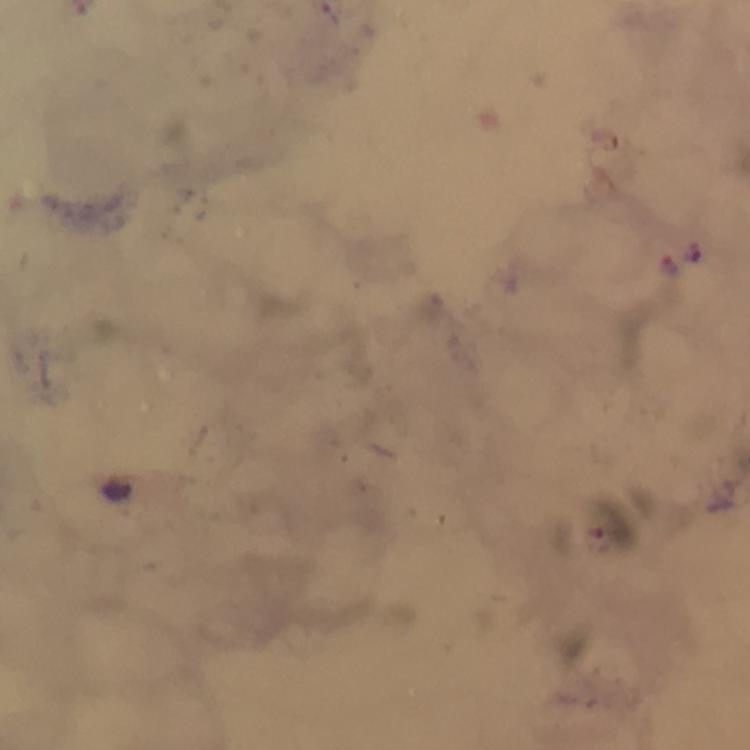
capture: smartphone camera through the microscope
immersion_oil: applied
plasmodium_parasite_locations: 'approximate centers as (x, y) in pixels: (667, 265)'
cropped_from: a single field of view
context: from a malaria diagnostic workup
preparation: thick blood smear
magnification: 100x
image_size: 750×750 pixels
stain: Giemsa